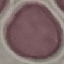
malaria status = uninfected
capture = smartphone camera at the microscope eyepiece
stain = Giemsa
image type = cell patch, automatically extracted from a larger field of view and resized to 64 × 64 pixels
preparation = thin blood film